Identify the parasite.
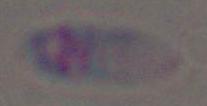
Toxoplasma gondii.

magnification = 1000x
modality = micrograph